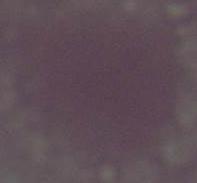
identification = erythrocyte
modality = photomicrograph
magnification = 1000x